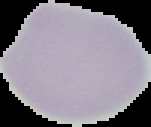
Summary:
  - Image size: 151×127 pixels
  - Preparation: thin blood smear
  - Result: negative for malaria parasites
  - Image type: cell region segmented out of the field of view; surrounding area masked to black